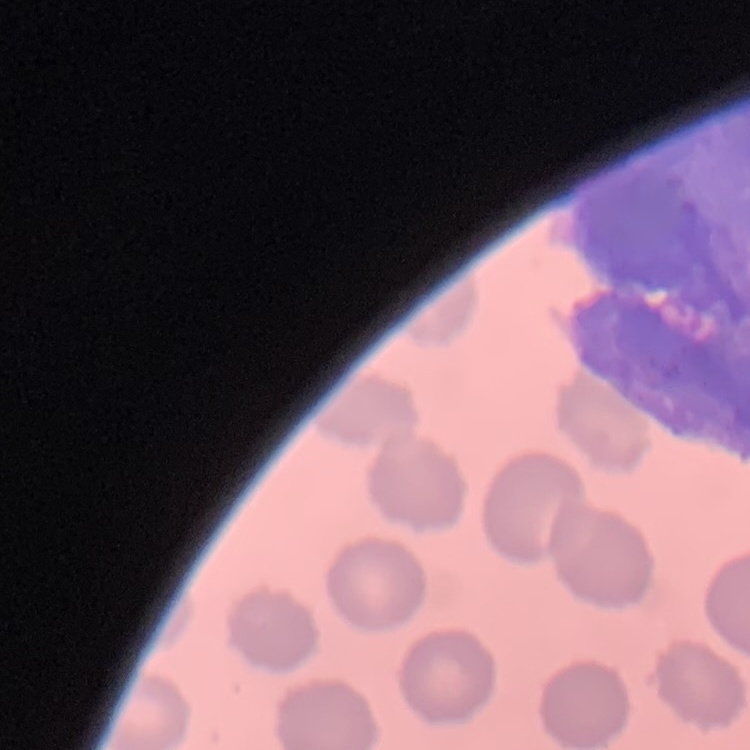
The erythrocytes exhibit no rouleaux formation. Stained with either Field's or Giemsa. Square crop of a larger photomicrograph. Thin blood film.